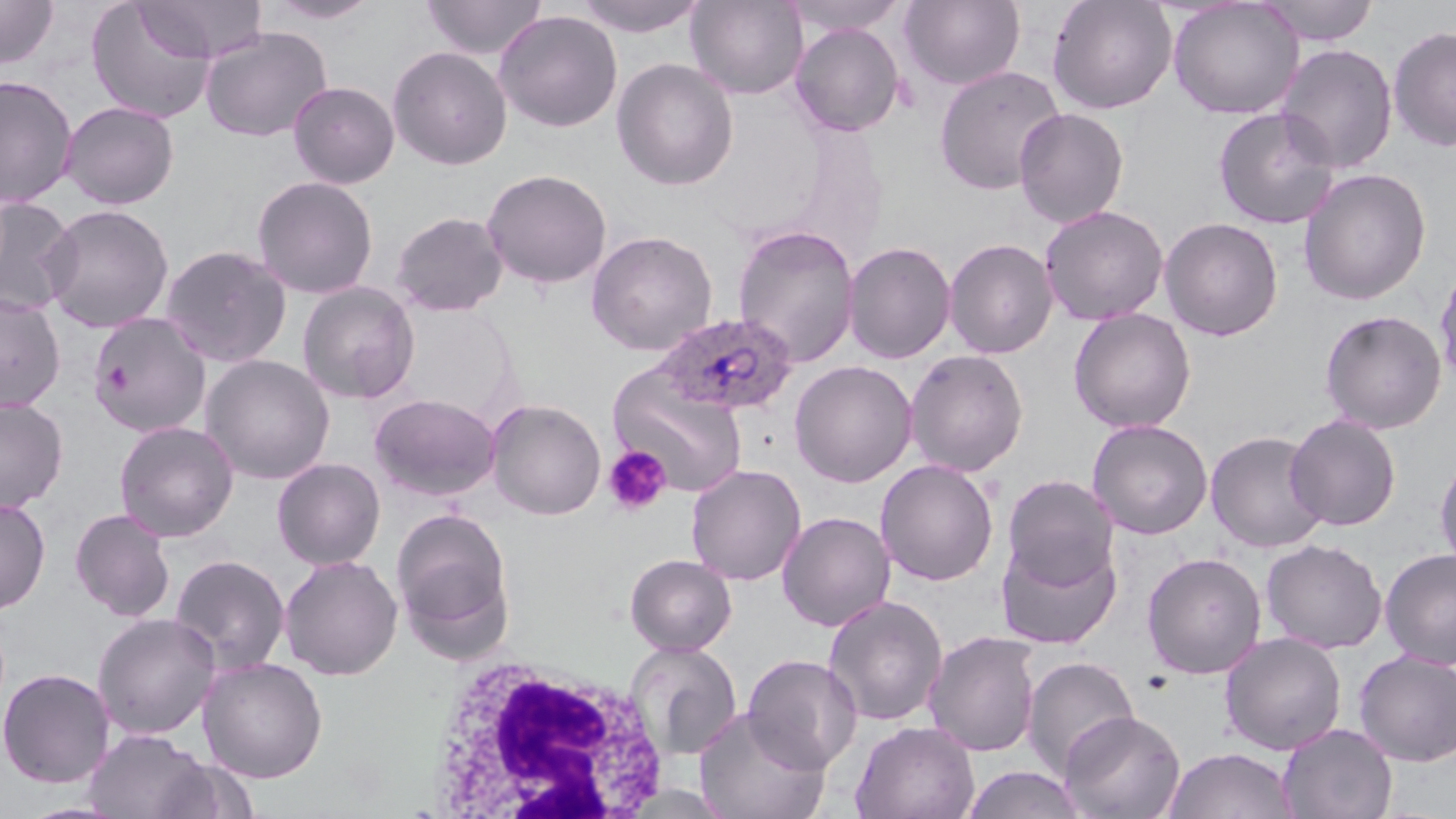

Summary:
  - Coordinate format: approximate bounding boxes as named x1/y1/x2/y2 corners in pixels
  - Platelet locations: (x1=602, y1=444, x2=672, y2=516)
  - Uninfected red blood cell locations: (x1=0, y1=0, x2=59, y2=69), (x1=263, y1=0, x2=383, y2=24), (x1=421, y1=0, x2=547, y2=60), (x1=572, y1=0, x2=709, y2=37), (x1=686, y1=0, x2=808, y2=99), (x1=783, y1=0, x2=908, y2=36), (x1=899, y1=0, x2=1026, y2=91), (x1=1047, y1=0, x2=1177, y2=115), (x1=1168, y1=0, x2=1304, y2=119), (x1=1256, y1=0, x2=1380, y2=46), (x1=85, y1=1, x2=217, y2=123), (x1=134, y1=1, x2=268, y2=63), (x1=494, y1=10, x2=623, y2=132), (x1=790, y1=23, x2=905, y2=137), (x1=1387, y1=25, x2=1456, y2=152), (x1=200, y1=26, x2=332, y2=143), (x1=1275, y1=44, x2=1398, y2=174), (x1=388, y1=46, x2=512, y2=170), (x1=611, y1=58, x2=739, y2=190), (x1=935, y1=65, x2=1066, y2=196), (x1=0, y1=75, x2=78, y2=208), (x1=288, y1=81, x2=399, y2=188), (x1=61, y1=101, x2=179, y2=209), (x1=1013, y1=107, x2=1129, y2=228), (x1=1212, y1=107, x2=1341, y2=230), (x1=1297, y1=167, x2=1432, y2=306), (x1=481, y1=169, x2=612, y2=289), (x1=252, y1=175, x2=379, y2=299), (x1=0, y1=197, x2=78, y2=316), (x1=40, y1=203, x2=175, y2=333), (x1=1039, y1=205, x2=1169, y2=325), (x1=390, y1=211, x2=509, y2=317), (x1=1159, y1=217, x2=1283, y2=341), (x1=732, y1=224, x2=860, y2=368), (x1=586, y1=230, x2=718, y2=356), (x1=944, y1=238, x2=1058, y2=359), (x1=842, y1=241, x2=957, y2=364), (x1=159, y1=244, x2=293, y2=368), (x1=1434, y1=259, x2=1456, y2=390), (x1=297, y1=282, x2=420, y2=404), (x1=0, y1=293, x2=66, y2=412), (x1=1068, y1=307, x2=1197, y2=434), (x1=1320, y1=310, x2=1446, y2=434), (x1=87, y1=312, x2=212, y2=437), (x1=904, y1=349, x2=1029, y2=477), (x1=200, y1=353, x2=335, y2=484), (x1=789, y1=360, x2=918, y2=488), (x1=607, y1=365, x2=749, y2=496), (x1=369, y1=393, x2=501, y2=502), (x1=0, y1=398, x2=68, y2=513), (x1=485, y1=398, x2=607, y2=520), (x1=1285, y1=413, x2=1401, y2=531), (x1=1086, y1=419, x2=1213, y2=540), (x1=114, y1=421, x2=239, y2=542), (x1=1205, y1=430, x2=1329, y2=553), (x1=1434, y1=452, x2=1456, y2=574), (x1=272, y1=457, x2=386, y2=570), (x1=875, y1=459, x2=999, y2=586), (x1=685, y1=463, x2=806, y2=586), (x1=1002, y1=474, x2=1119, y2=587), (x1=0, y1=498, x2=51, y2=614), (x1=391, y1=506, x2=515, y2=652), (x1=70, y1=508, x2=176, y2=622), (x1=777, y1=511, x2=896, y2=632), (x1=996, y1=535, x2=1122, y2=650), (x1=1261, y1=538, x2=1388, y2=654), (x1=1380, y1=548, x2=1456, y2=669), (x1=1141, y1=552, x2=1267, y2=679), (x1=624, y1=553, x2=737, y2=656), (x1=169, y1=554, x2=290, y2=675), (x1=278, y1=554, x2=403, y2=681), (x1=823, y1=594, x2=948, y2=727), (x1=92, y1=612, x2=221, y2=739), (x1=923, y1=631, x2=1042, y2=757), (x1=1220, y1=632, x2=1346, y2=755), (x1=625, y1=641, x2=742, y2=760), (x1=1354, y1=650, x2=1456, y2=766), (x1=742, y1=654, x2=863, y2=773), (x1=198, y1=656, x2=328, y2=783), (x1=1021, y1=656, x2=1140, y2=779), (x1=0, y1=668, x2=115, y2=788), (x1=693, y1=706, x2=831, y2=819), (x1=1060, y1=709, x2=1186, y2=819), (x1=850, y1=720, x2=979, y2=819), (x1=1278, y1=723, x2=1397, y2=819), (x1=83, y1=729, x2=212, y2=819), (x1=1163, y1=747, x2=1298, y2=819), (x1=154, y1=759, x2=260, y2=818), (x1=961, y1=765, x2=1088, y2=819)
  - White blood cell locations: (x1=423, y1=658, x2=672, y2=815)
  - Plasmodium ovale-infected red blood cell locations: (x1=654, y1=312, x2=799, y2=417)
  - Slide-level diagnosis: Plasmodium ovale
  - Field of view: one of a larger specimen
  - Preparation: thin blood film
  - Modality: light microscopy
  - Stain: May-Grünwald-Giemsa
  - Image size: 1456×819 pixels
  - Magnification: 1000x